Name the blood parasite species.
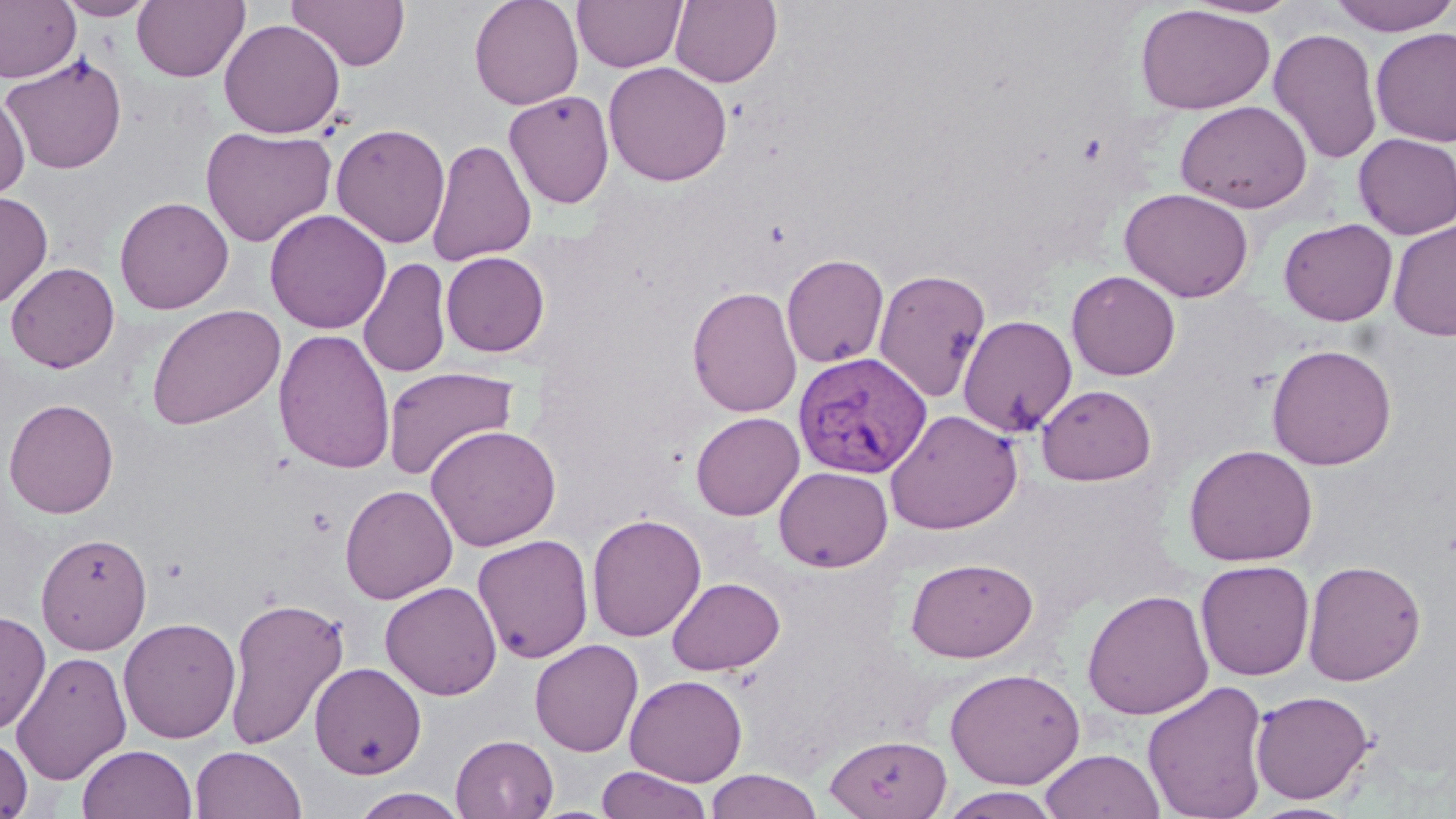

Plasmodium vivax.

Summary:
  - Coordinate format: approximate bounding boxes as (x1,y1)-(x2,y2) corner pairs in pixels
  - Plasmodium vivax-infected red blood cell locations: (793,351)-(932,479)
  - Uninfected red blood cell locations: (0,0)-(81,83), (55,0)-(157,20), (132,0)-(249,83), (287,0)-(410,71), (469,0)-(584,110), (572,0)-(687,72), (670,0)-(782,87), (1183,0)-(1302,19), (1329,0)-(1456,36), (1135,4)-(1276,115), (219,18)-(345,139), (1268,27)-(1383,165), (1370,27)-(1456,146), (1,54)-(128,174), (603,61)-(733,186), (504,90)-(615,209), (0,91)-(31,202), (1175,100)-(1313,213), (330,123)-(451,248), (200,126)-(336,248), (1353,133)-(1456,239), (426,139)-(537,267), (1119,187)-(1254,302), (0,190)-(53,310), (114,196)-(234,314), (265,209)-(391,334), (1278,218)-(1398,326), (1387,220)-(1456,341), (441,251)-(549,357), (781,253)-(889,368), (357,257)-(452,378), (5,261)-(120,373), (873,268)-(991,403), (1066,271)-(1181,380), (687,285)-(803,418), (146,304)-(286,430), (957,314)-(1077,437), (273,328)-(396,474), (1266,343)-(1398,470), (382,365)-(519,481), (1036,384)-(1157,485), (3,398)-(119,519), (884,409)-(1023,534), (690,411)-(804,520), (425,424)-(561,551), (1183,443)-(1318,566), (774,466)-(893,572), (340,484)-(457,604), (586,513)-(706,642), (35,532)-(153,654), (472,533)-(594,663), (906,557)-(1038,662), (1303,559)-(1426,686), (1195,560)-(1315,681), (667,577)-(785,676), (380,581)-(502,700), (1081,589)-(1214,720), (223,594)-(350,751), (0,609)-(51,735), (118,617)-(241,744), (529,639)-(644,757), (10,650)-(132,784), (310,661)-(427,779), (945,667)-(1085,790), (625,674)-(747,786), (1142,680)-(1270,819), (1250,689)-(1374,804), (0,734)-(33,818), (451,734)-(559,818), (824,734)-(952,818), (77,744)-(197,819), (191,746)-(307,819), (1039,748)-(1165,819), (596,765)-(713,819), (705,769)-(824,819), (347,787)-(471,818), (938,788)-(1063,819), (1247,801)-(1360,819)
  - Magnification: 1000x
  - Modality: optical microscopy
  - Stain: May-Grünwald-Giemsa
  - Image size: 1456×819 pixels
  - Preparation: thin blood film
  - Field of view: one of a larger specimen